Assess this cell for malaria.
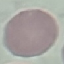

Uninfected.

Summary:
  - Preparation: thin blood film
  - Capture: smartphone camera at the microscope eyepiece
  - Stain: Giemsa
  - Image type: automatically extracted cell patch, resized to 64 × 64 pixels